Assess this cell for malaria.
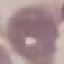
It is uninfected.

preparation = thin blood film
capture = smartphone camera at the microscope eyepiece
stain = Giemsa
image type = automatically extracted cell patch, resized to 64 × 64 pixels